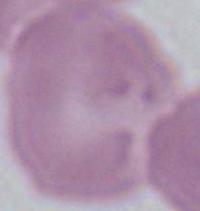
magnification = 1000x
modality = micrograph
identification = red blood cell